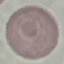
Summary:
  - Malaria status: uninfected
  - Image type: automatically extracted cell patch, resized to 64 × 64 pixels
  - Capture: smartphone camera at the microscope eyepiece
  - Stain: Giemsa
  - Preparation: thin smear